Mark where platelets are.
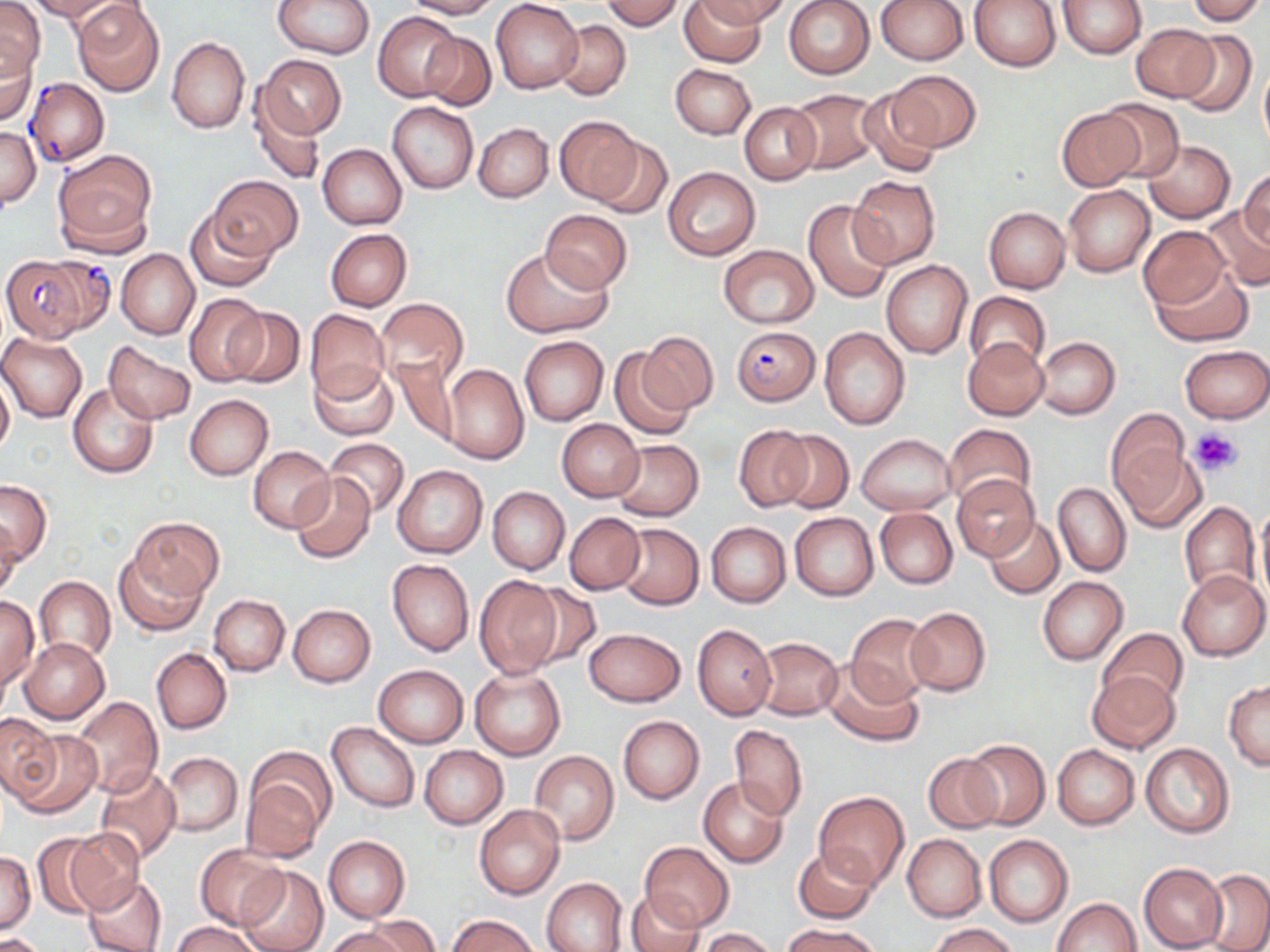

Approximate bounding boxes as (x1, y1, x2, y2) in pixels.
Platelets: (1190, 427, 1243, 477).

Plasmodium falciparum-infected red blood cell locations = approximate bounding boxes as (x1, y1, x2, y2) in pixels: (25, 78, 109, 167), (1, 253, 112, 343), (729, 324, 820, 405)
slide-level diagnosis = Plasmodium falciparum
image size = 1270×952 pixels
magnification = 1000x
uninfected red blood cell locations = approximate bounding boxes as (x1, y1, x2, y2) in pixels: (29, 0, 119, 21), (73, 0, 167, 97), (274, 0, 374, 58), (403, 0, 499, 19), (492, 0, 583, 93), (599, 0, 684, 30), (679, 0, 766, 66), (695, 0, 791, 27), (784, 0, 875, 79), (875, 0, 968, 65), (969, 0, 1060, 72), (1056, 0, 1146, 58), (1185, 0, 1266, 25), (0, 1, 44, 81), (374, 11, 461, 101), (553, 20, 630, 100), (1132, 22, 1217, 102), (1175, 30, 1257, 119), (420, 31, 496, 110), (167, 36, 250, 133), (0, 44, 38, 126), (258, 55, 345, 139), (1259, 61, 1270, 157), (670, 63, 756, 139), (887, 69, 980, 152), (858, 87, 945, 179), (788, 88, 882, 173), (250, 91, 324, 186), (1099, 100, 1186, 181), (388, 101, 478, 194), (739, 102, 821, 184), (1055, 108, 1145, 191), (555, 117, 642, 204), (473, 122, 553, 202), (1, 127, 40, 206), (592, 138, 672, 220), (1143, 140, 1234, 223), (318, 144, 406, 230), (52, 149, 156, 252), (662, 167, 760, 261), (1239, 167, 1269, 247), (209, 176, 302, 259), (849, 177, 940, 268), (1063, 184, 1156, 278), (803, 201, 894, 303), (1204, 204, 1270, 293), (984, 207, 1070, 293), (186, 209, 276, 292), (539, 210, 632, 292), (1137, 225, 1229, 309), (326, 228, 412, 311), (718, 245, 819, 328), (503, 247, 613, 338), (116, 249, 199, 340), (880, 260, 973, 359), (1149, 266, 1252, 345), (963, 292, 1051, 373), (185, 294, 268, 387), (374, 299, 469, 391), (226, 306, 304, 388), (305, 308, 390, 402), (819, 326, 910, 429), (639, 331, 718, 413), (0, 334, 88, 421), (519, 336, 608, 426), (962, 337, 1048, 420), (1034, 337, 1119, 420), (105, 341, 195, 424), (1179, 344, 1270, 422), (608, 348, 694, 441), (390, 357, 460, 445), (310, 363, 397, 440), (441, 363, 529, 466), (0, 374, 14, 455), (68, 384, 159, 479), (184, 395, 273, 480), (1106, 409, 1189, 496), (558, 419, 643, 501), (942, 423, 1036, 508), (735, 424, 814, 511), (777, 429, 853, 514), (855, 434, 957, 515), (1111, 437, 1202, 530), (325, 438, 409, 517), (612, 439, 704, 521), (248, 445, 335, 532), (392, 464, 488, 558), (289, 472, 377, 564), (951, 474, 1039, 561), (1, 479, 52, 564), (1052, 480, 1130, 577), (487, 487, 568, 574), (1178, 501, 1260, 598), (1254, 503, 1270, 610), (875, 508, 958, 588), (565, 512, 645, 594), (790, 512, 878, 602), (130, 516, 222, 603), (985, 517, 1064, 598), (0, 521, 22, 601), (707, 522, 790, 608), (616, 524, 704, 610), (114, 551, 207, 636), (387, 558, 474, 656), (1178, 570, 1269, 661), (472, 574, 563, 680), (34, 576, 115, 662), (1037, 577, 1127, 664), (522, 579, 601, 669), (209, 595, 289, 676), (0, 596, 39, 690), (288, 604, 375, 687), (904, 607, 990, 696), (846, 613, 936, 707), (693, 623, 777, 720), (584, 628, 686, 706), (1100, 628, 1188, 707), (19, 637, 109, 722), (754, 637, 842, 720), (152, 648, 231, 734), (820, 660, 922, 746), (372, 663, 469, 748), (469, 665, 565, 760), (1086, 670, 1179, 753), (1224, 681, 1270, 769), (72, 696, 162, 798), (0, 712, 58, 798), (618, 716, 704, 803), (328, 722, 420, 812), (730, 724, 807, 820), (11, 728, 101, 818), (962, 739, 1049, 829), (1140, 743, 1234, 837), (1052, 745, 1140, 829), (420, 746, 508, 830), (530, 749, 618, 845), (161, 752, 242, 835), (923, 752, 1004, 833), (95, 766, 181, 865), (241, 767, 329, 861), (697, 777, 789, 867), (814, 791, 908, 891), (473, 805, 565, 900), (63, 827, 146, 913), (902, 835, 986, 921), (984, 835, 1073, 927), (33, 836, 106, 917), (323, 836, 410, 922), (641, 841, 733, 931), (793, 845, 879, 923), (194, 846, 288, 929), (1, 852, 36, 935), (1138, 863, 1227, 952), (236, 866, 328, 952), (1201, 869, 1270, 952), (82, 875, 168, 952), (542, 877, 627, 952), (623, 887, 704, 951), (1051, 897, 1141, 952), (447, 913, 539, 952), (363, 916, 441, 952), (171, 920, 263, 952), (782, 922, 884, 952), (927, 923, 1021, 952), (325, 926, 411, 952), (698, 928, 777, 952), (0, 933, 49, 952)
stain = May-Grünwald-Giemsa
modality = light microscopy
field of view = one of a larger specimen
preparation = thin blood smear